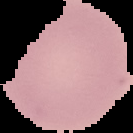
result = no Plasmodium parasites detected
image size = 133×133 pixels
preparation = thin blood film
image type = segmented cell region on a black background